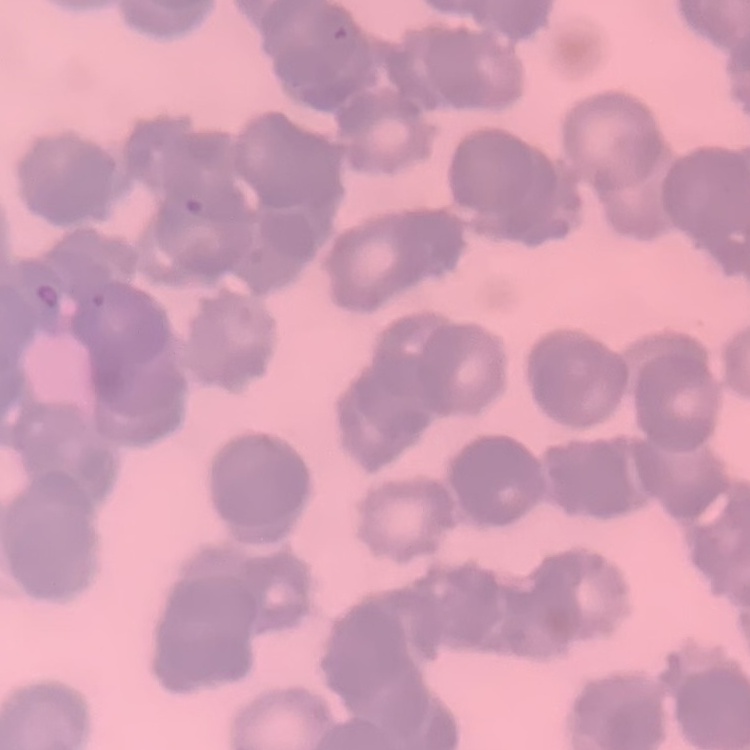

{
  "red_blood_cell_morphology": "rouleaux formation",
  "preparation": "thin peripheral smear",
  "image_type": "one tile cut from a larger photomicrograph",
  "stain": "Field's or Giemsa"
}